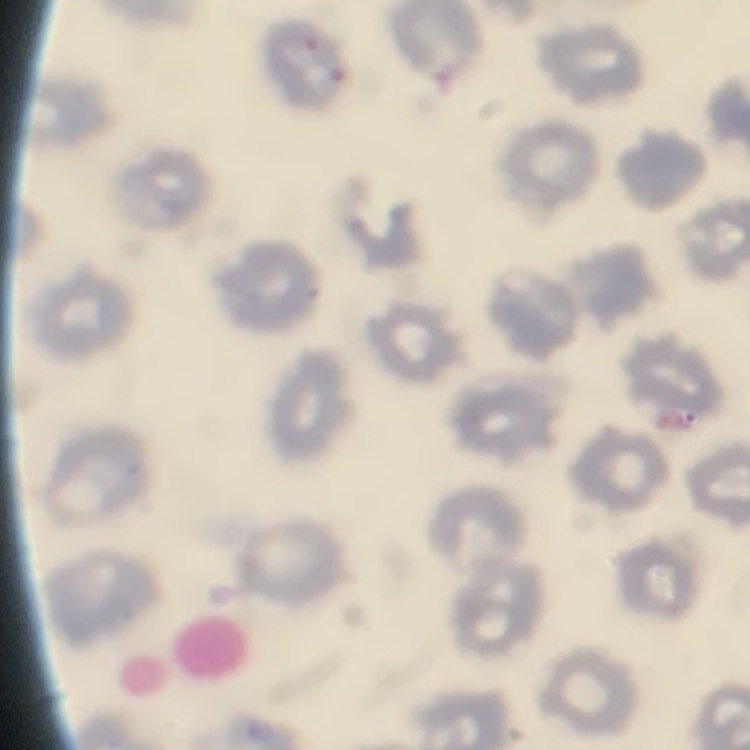
Summary:
  - Red blood cell morphology: no rouleaux formation
  - Preparation: thin peripheral smear
  - Image type: one tile cut from a larger photomicrograph
  - Stain: Field's or Giemsa